Locate every blood parasite and identify its species.
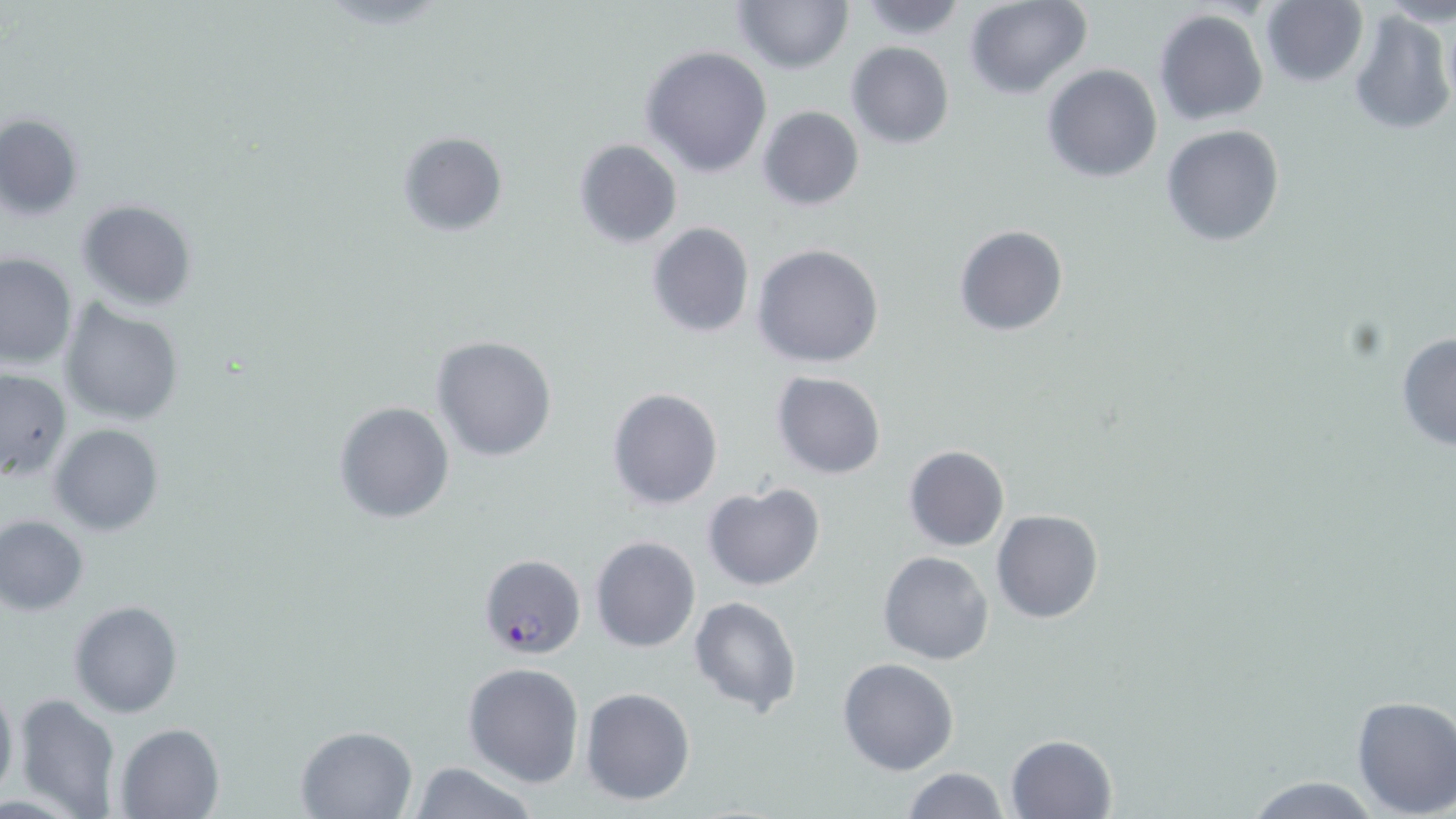
Approximate bounding boxes as named x1/y1/x2/y2 corners in pixels.
Plasmodium falciparum-infected red blood cells: (x1=478, y1=553, x2=585, y2=660).
No Plasmodium ovale, Plasmodium malariae, Plasmodium vivax, Babesia divergens, or Trypanosoma brucei observed.

{
  "slide_level_diagnosis": "Plasmodium falciparum",
  "magnification": "1000x",
  "uninfected_red_blood_cell_locations": "approximate bounding boxes as named x1/y1/x2/y2 corners in pixels: (x1=854, y1=0, x2=969, y2=41), (x1=964, y1=0, x2=1094, y2=99), (x1=733, y1=1, x2=853, y2=75), (x1=1262, y1=1, x2=1369, y2=88), (x1=1381, y1=2, x2=1456, y2=29), (x1=1346, y1=8, x2=1455, y2=135), (x1=1153, y1=9, x2=1269, y2=127), (x1=845, y1=41, x2=955, y2=150), (x1=642, y1=45, x2=772, y2=178), (x1=1042, y1=64, x2=1164, y2=184), (x1=757, y1=106, x2=864, y2=211), (x1=2, y1=112, x2=85, y2=221), (x1=1161, y1=125, x2=1287, y2=247), (x1=396, y1=131, x2=507, y2=237), (x1=574, y1=139, x2=683, y2=249), (x1=75, y1=198, x2=197, y2=312), (x1=645, y1=222, x2=754, y2=338), (x1=954, y1=225, x2=1069, y2=336), (x1=753, y1=242, x2=885, y2=369), (x1=0, y1=253, x2=76, y2=370), (x1=61, y1=302, x2=184, y2=426), (x1=1395, y1=332, x2=1456, y2=453), (x1=432, y1=335, x2=559, y2=463), (x1=0, y1=368, x2=71, y2=481), (x1=771, y1=371, x2=887, y2=479), (x1=607, y1=387, x2=724, y2=511), (x1=334, y1=400, x2=455, y2=522), (x1=48, y1=423, x2=164, y2=536), (x1=903, y1=446, x2=1009, y2=552), (x1=701, y1=483, x2=826, y2=592), (x1=990, y1=508, x2=1103, y2=624), (x1=1, y1=514, x2=89, y2=615), (x1=590, y1=536, x2=702, y2=654), (x1=878, y1=551, x2=995, y2=665), (x1=688, y1=595, x2=804, y2=719), (x1=68, y1=600, x2=183, y2=718), (x1=837, y1=657, x2=959, y2=775), (x1=462, y1=662, x2=584, y2=789), (x1=0, y1=681, x2=19, y2=802), (x1=579, y1=686, x2=697, y2=806), (x1=13, y1=693, x2=121, y2=819), (x1=1348, y1=695, x2=1456, y2=818), (x1=115, y1=722, x2=224, y2=819), (x1=295, y1=724, x2=418, y2=817), (x1=1006, y1=734, x2=1118, y2=819), (x1=404, y1=762, x2=542, y2=819), (x1=898, y1=766, x2=1011, y2=819), (x1=1237, y1=776, x2=1390, y2=818)",
  "modality": "light microscopy",
  "stain": "May-Grünwald-Giemsa",
  "preparation": "thin blood film",
  "field_of_view": "one of a larger specimen",
  "image_size": "1456×819 pixels"
}